Report the malaria status of this cell.
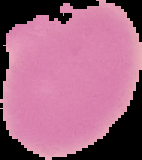
Uninfected.

From a thin blood film. The area outside the segmented cell region is set to black. Image is 142×160 pixels.